Point out each malaria parasite and each leukocyte.
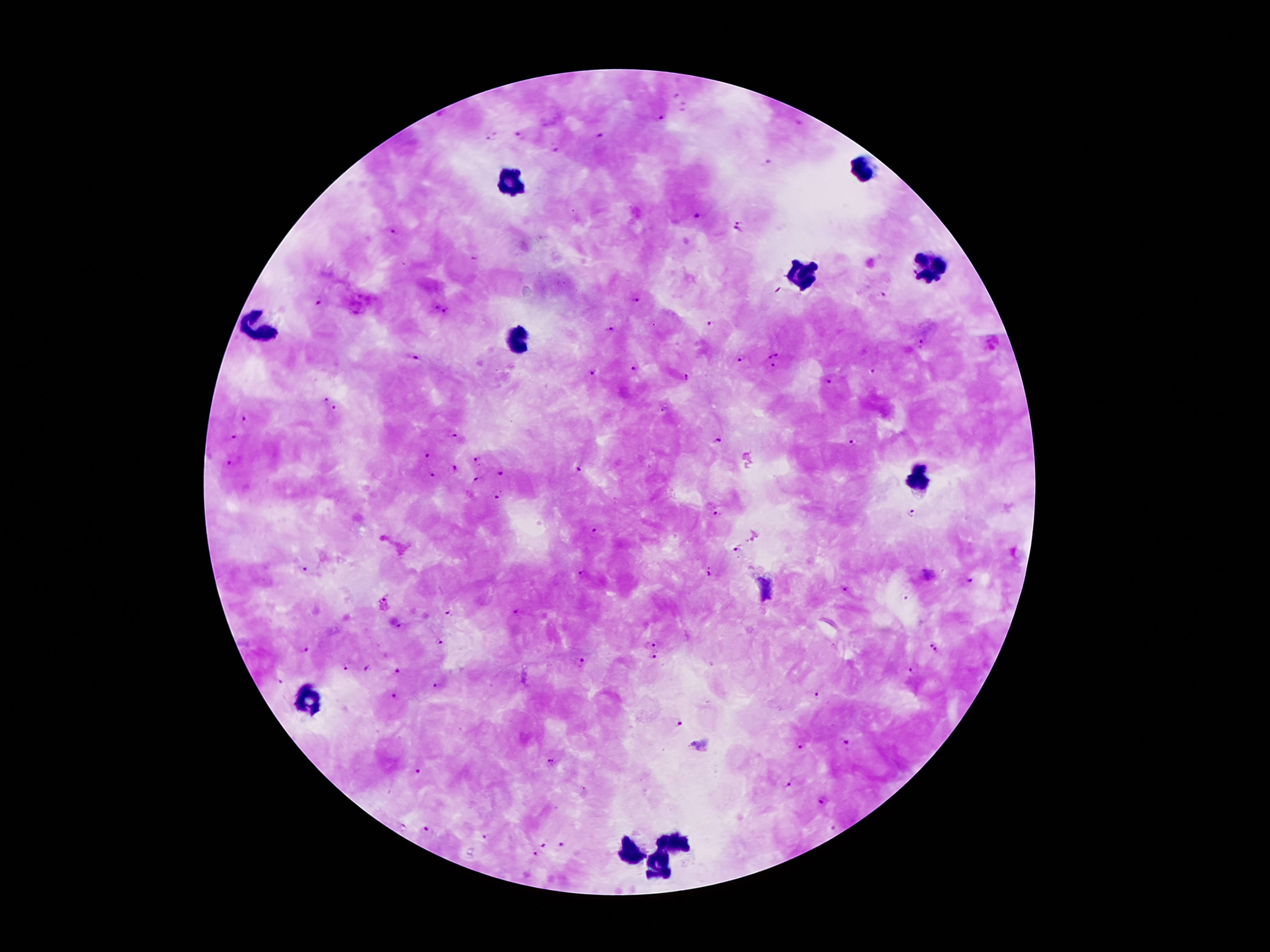

Approximate object centers, in pixels from the top-left corner.
Malaria parasites: (x=663, y=117), (x=798, y=124), (x=519, y=134), (x=598, y=136), (x=490, y=138), (x=556, y=150), (x=769, y=162), (x=699, y=216), (x=738, y=220), (x=396, y=232), (x=736, y=233), (x=476, y=259), (x=881, y=294), (x=634, y=301), (x=320, y=304), (x=435, y=306), (x=446, y=311), (x=710, y=325), (x=608, y=330), (x=921, y=344), (x=778, y=353), (x=414, y=357), (x=768, y=357), (x=741, y=359), (x=773, y=368), (x=632, y=370), (x=873, y=371), (x=593, y=373), (x=687, y=378), (x=828, y=381), (x=326, y=399), (x=336, y=411), (x=242, y=419), (x=454, y=437), (x=234, y=438), (x=716, y=441), (x=852, y=442), (x=426, y=455), (x=479, y=460), (x=229, y=463), (x=455, y=469), (x=579, y=471), (x=500, y=474), (x=431, y=476), (x=476, y=479), (x=495, y=499), (x=718, y=513), (x=914, y=513), (x=596, y=532), (x=736, y=551), (x=304, y=569), (x=708, y=571), (x=581, y=573), (x=927, y=574), (x=968, y=583), (x=844, y=588), (x=447, y=613), (x=398, y=627), (x=440, y=642), (x=930, y=643), (x=650, y=644), (x=303, y=650), (x=936, y=653), (x=655, y=660), (x=581, y=662), (x=345, y=669), (x=367, y=669), (x=398, y=670), (x=912, y=671), (x=278, y=681), (x=438, y=686), (x=814, y=692), (x=393, y=696), (x=679, y=725), (x=846, y=744), (x=799, y=745), (x=550, y=762), (x=418, y=770), (x=788, y=784), (x=821, y=800), (x=837, y=828), (x=426, y=831), (x=483, y=837), (x=544, y=844), (x=562, y=846), (x=533, y=854).
Leukocytes: (x=865, y=168), (x=507, y=186), (x=934, y=270), (x=801, y=274), (x=262, y=327), (x=520, y=340), (x=920, y=477), (x=673, y=842), (x=628, y=848), (x=659, y=864).

image size = 1270×952 pixels
preparation = thick blood smear
capture = smartphone through the microscope eyepiece
stain = Giemsa
field of view = single
patient malaria status = positive for Plasmodium falciparum
magnification = 100x